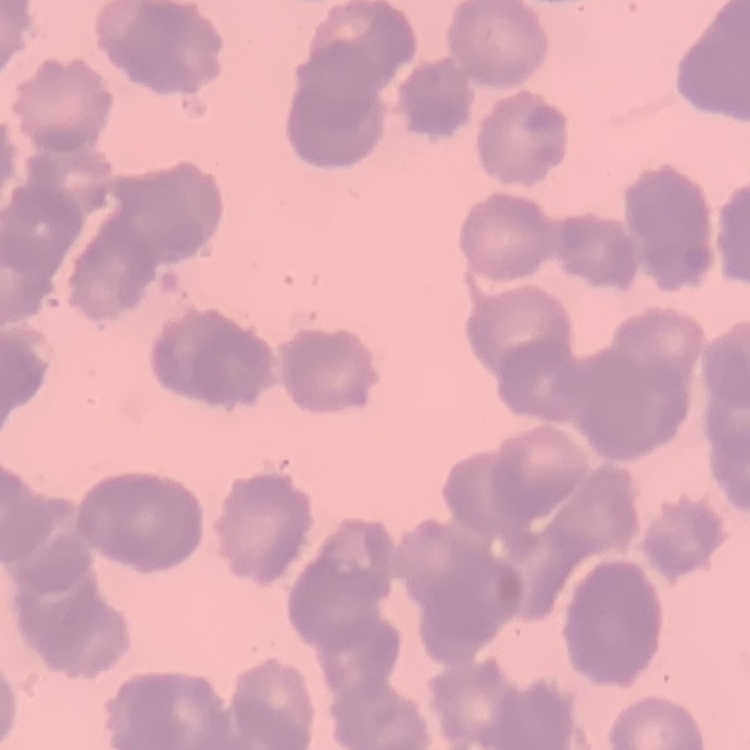

Summary:
  - Red blood cell morphology: rouleaux formation
  - Stain: Field's or Giemsa
  - Preparation: thin blood smear
  - Image type: square crop of a larger photomicrograph